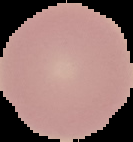

{
  "image_size": "133×142 pixels",
  "malaria_status": "uninfected",
  "preparation": "thin blood film",
  "image_type": "segmented cell region with the area outside set to black"
}